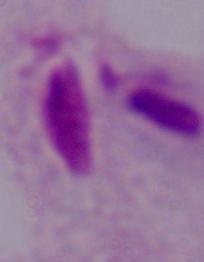
Captured at 1000x magnification. A trichomonad is shown. Micrograph.